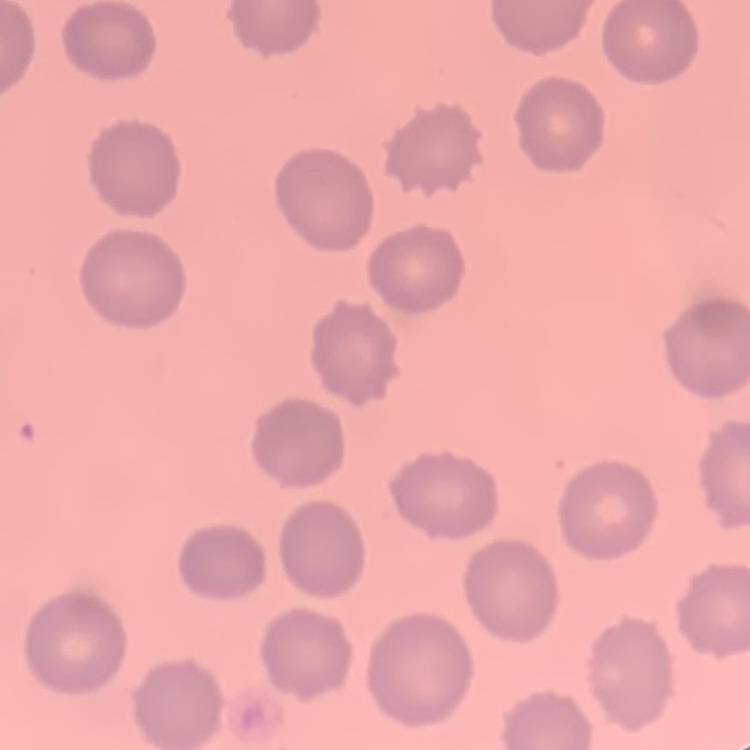
red blood cell morphology = no rouleaux formation
image type = square crop of a larger photomicrograph
stain = Field's or Giemsa
preparation = thin blood smear